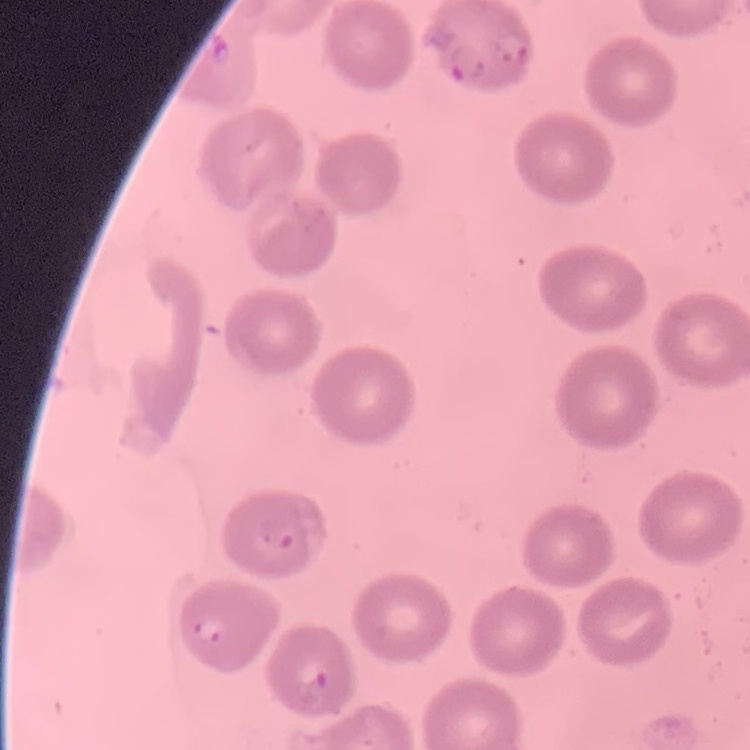
red blood cell morphology = no rouleaux formation
image type = square crop of a larger photomicrograph
preparation = thin blood film
stain = Field's or Giemsa